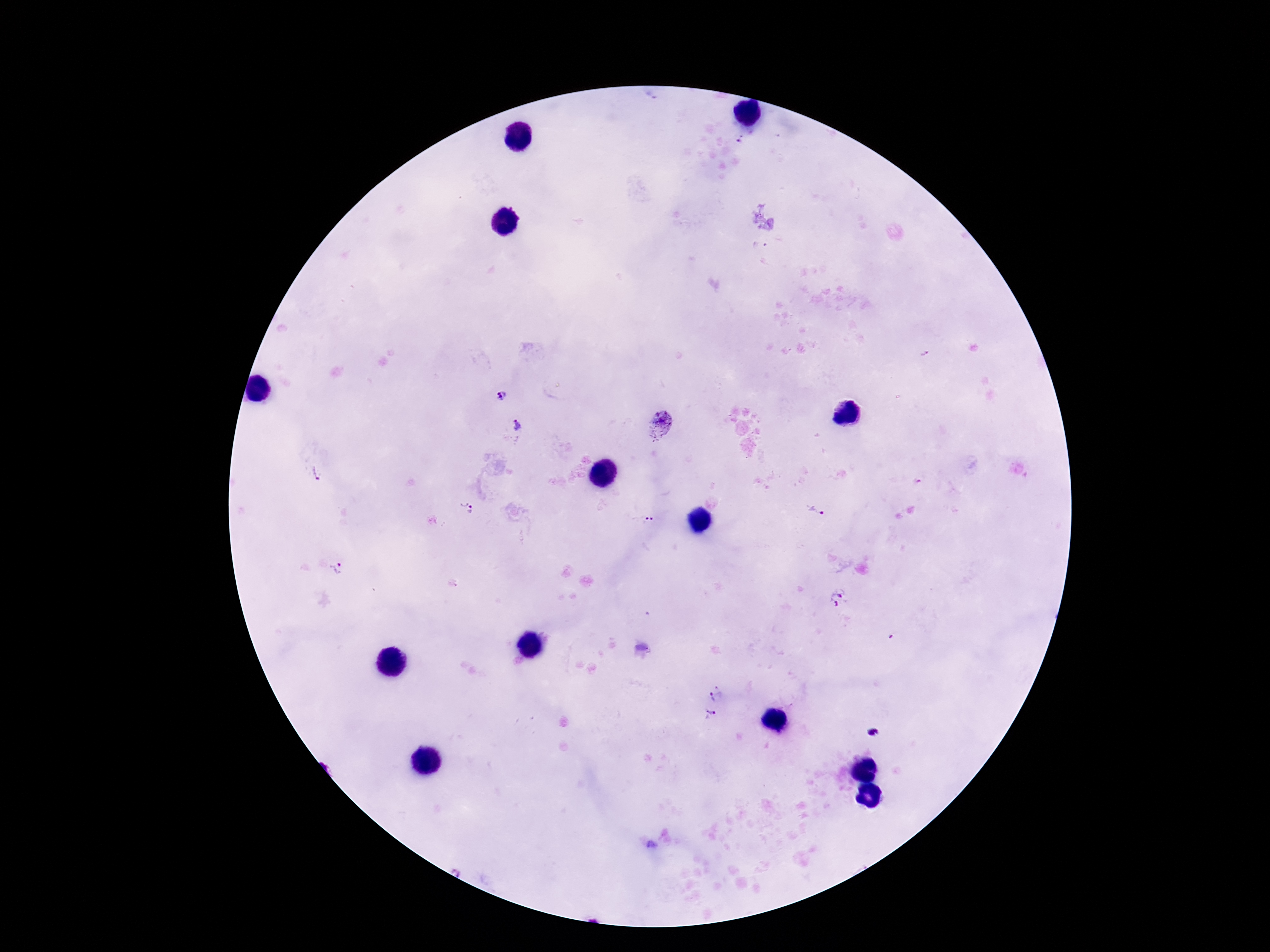

Approximate object centers, in pixels from the top-left corner.
Summary:
  - Plasmodium parasite locations: (x=500, y=395), (x=516, y=425), (x=660, y=426), (x=316, y=475), (x=465, y=509), (x=815, y=512), (x=643, y=517), (x=337, y=569), (x=838, y=598), (x=716, y=693), (x=710, y=716), (x=872, y=732), (x=651, y=844)
  - Magnification: 100x
  - Field of view: one from this slide
  - Capture: smartphone camera through the microscope eyepiece
  - Patient malaria status: infected
  - Image size: 1270×952 pixels
  - Stain: Giemsa
  - Preparation: thick peripheral-blood smear